Point out each Plasmodium parasite.
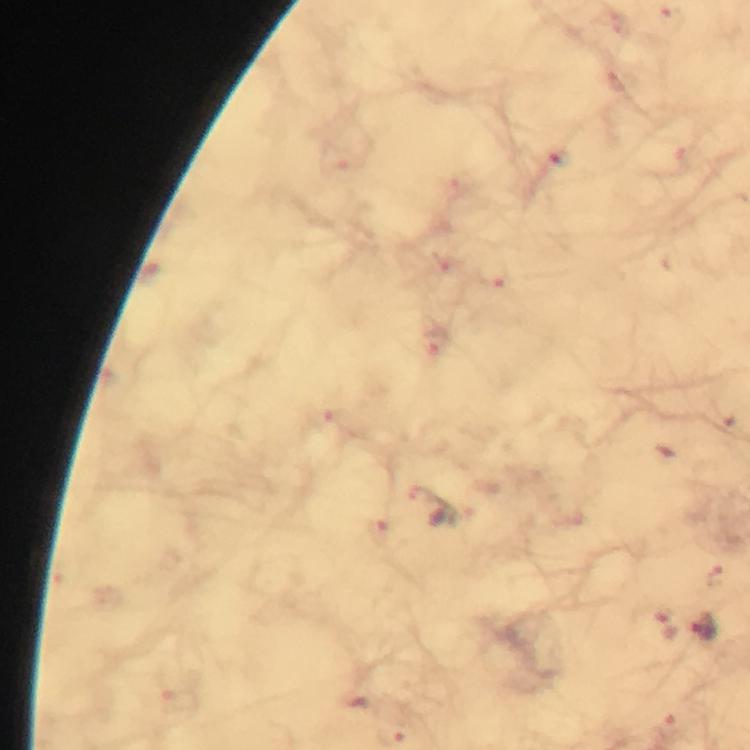
Approximate object centers, in pixels from the top-left corner.
Plasmodium parasites: (x=672, y=18), (x=558, y=158), (x=494, y=277), (x=716, y=576), (x=704, y=627).

At 100x magnification. Photographed through the microscope with a smartphone camera. Thick blood smear. Cropped region of a single field of view. Image is 750×750 pixels. Immersion oil was used. From a malaria diagnostic workup. Giemsa-stained preparation.